Identify the cell.
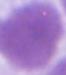

This is an erythrocyte.

modality = photomicrograph
magnification = 1000x